State which parasite is depicted.
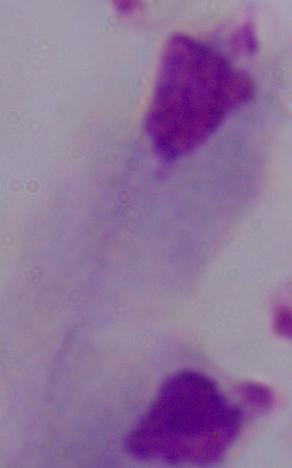
A trichomonad.

{
  "modality": "photomicrograph",
  "magnification": "1000x"
}